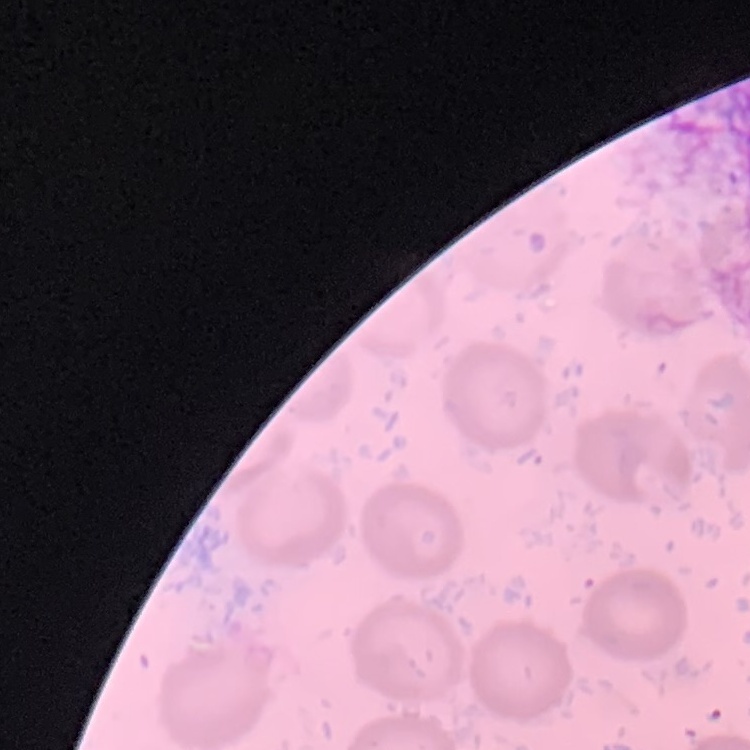

{
  "red_blood_cell_morphology": "no rouleaux formation",
  "stain": "Field's or Giemsa",
  "preparation": "thin peripheral smear",
  "image_type": "square crop of a larger photomicrograph"
}